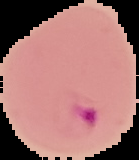
Summary:
  - Image type: segmented cell region on a black background
  - Image size: 139×160 pixels
  - Result: malaria parasites detected
  - Preparation: thin blood film